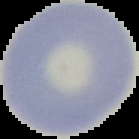

preparation = thin blood smear
image size = 139×139 pixels
image type = segmented cell region on a black background
malaria status = uninfected